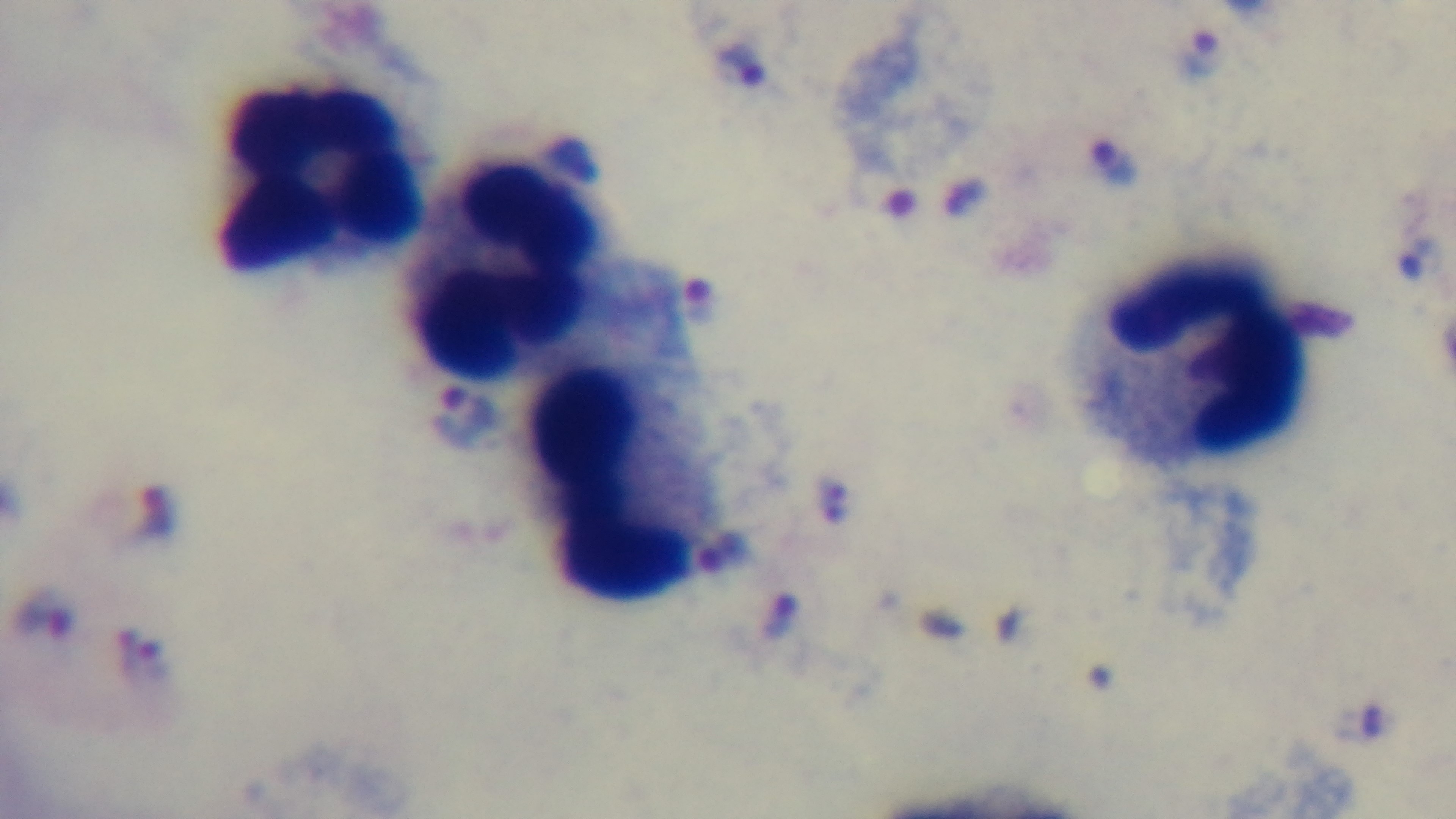
Malaria status: positive. Preparation: thick blood film. Giemsa-stained. Oil-immersion objective, 100x. Photomicrograph. Mounted 4K digital camera. One field from the slide.